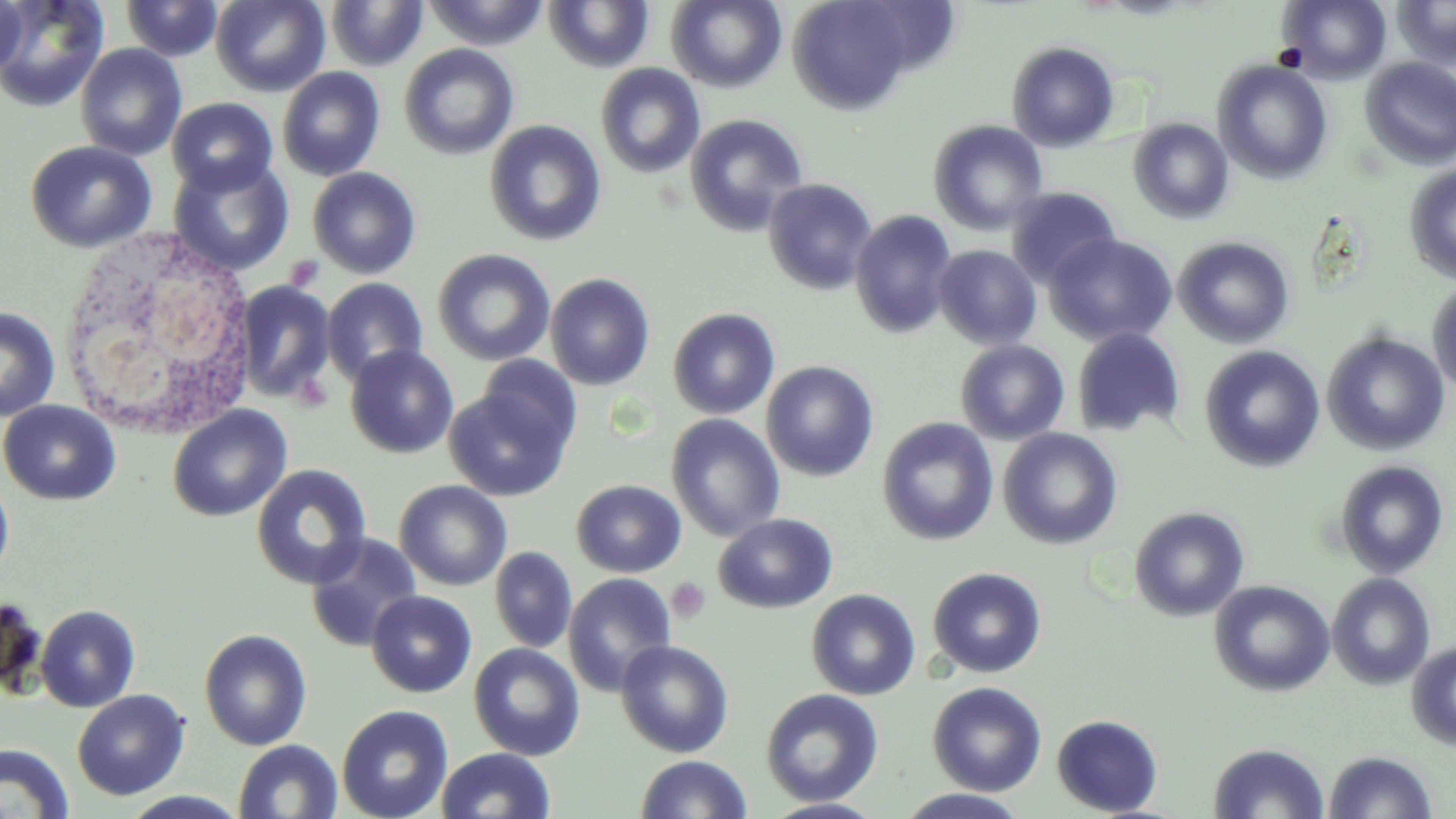

Approximate bounding boxes as (x1, y1, x2, y2) in pixels. White blood cell locations: (64, 218, 263, 447). Platelet locations: (285, 255, 325, 292), (293, 373, 333, 412), (667, 577, 712, 623). Uninfected red blood cell locations: (0, 0, 109, 112), (0, 0, 29, 81), (120, 0, 224, 62), (210, 0, 329, 96), (326, 0, 427, 70), (423, 0, 549, 50), (787, 0, 922, 115), (1278, 0, 1391, 84), (1392, 0, 1456, 71), (543, 1, 655, 72), (667, 1, 787, 92), (1007, 42, 1120, 151), (75, 43, 187, 161), (399, 43, 519, 160), (1359, 57, 1456, 169), (1212, 60, 1333, 184), (595, 63, 705, 179), (277, 67, 385, 181), (167, 97, 278, 196), (684, 114, 808, 237), (1128, 117, 1235, 224), (485, 120, 607, 246), (928, 120, 1049, 235), (25, 140, 157, 253), (168, 156, 294, 275), (1404, 164, 1456, 284), (307, 166, 421, 279), (763, 178, 878, 295), (1006, 187, 1122, 288), (850, 209, 957, 338), (1044, 233, 1177, 346), (1173, 236, 1295, 349), (933, 245, 1042, 350), (432, 249, 555, 366), (545, 273, 655, 390), (322, 277, 429, 385), (1427, 278, 1456, 398), (232, 281, 336, 403), (0, 305, 60, 421), (668, 307, 780, 419), (1072, 328, 1186, 437), (1322, 333, 1450, 455), (955, 340, 1070, 445), (345, 345, 459, 459), (1200, 345, 1325, 472), (473, 355, 584, 460), (761, 360, 879, 481), (444, 380, 576, 502), (0, 399, 121, 506), (168, 405, 291, 522), (666, 413, 785, 542), (878, 417, 998, 546), (998, 428, 1123, 550), (1334, 460, 1449, 578), (251, 464, 372, 589), (0, 470, 14, 580), (394, 479, 512, 591), (571, 479, 686, 577), (1129, 506, 1249, 622), (713, 513, 838, 614), (305, 533, 425, 652), (490, 547, 577, 653), (927, 567, 1047, 678), (563, 572, 677, 696), (1327, 573, 1436, 690), (1209, 579, 1335, 697), (806, 588, 921, 700), (366, 590, 477, 698), (0, 594, 46, 697), (35, 605, 140, 712), (199, 628, 312, 751), (1406, 639, 1456, 750), (616, 640, 734, 758), (469, 643, 585, 760), (927, 681, 1047, 796), (761, 688, 884, 807), (72, 690, 190, 800), (337, 704, 454, 818), (1051, 713, 1164, 816), (233, 739, 343, 818), (1208, 741, 1329, 819), (0, 742, 75, 819), (436, 747, 556, 819), (1323, 750, 1438, 818), (634, 754, 753, 818), (894, 789, 1034, 819), (120, 791, 250, 818), (760, 798, 889, 819). Slide-level diagnosis: no evidence of blood parasites. Image is 1456×819 pixels. May-Grünwald-Giemsa-stained preparation. Single field of view. Optical microscopy. Thin blood film. 1000x magnification.